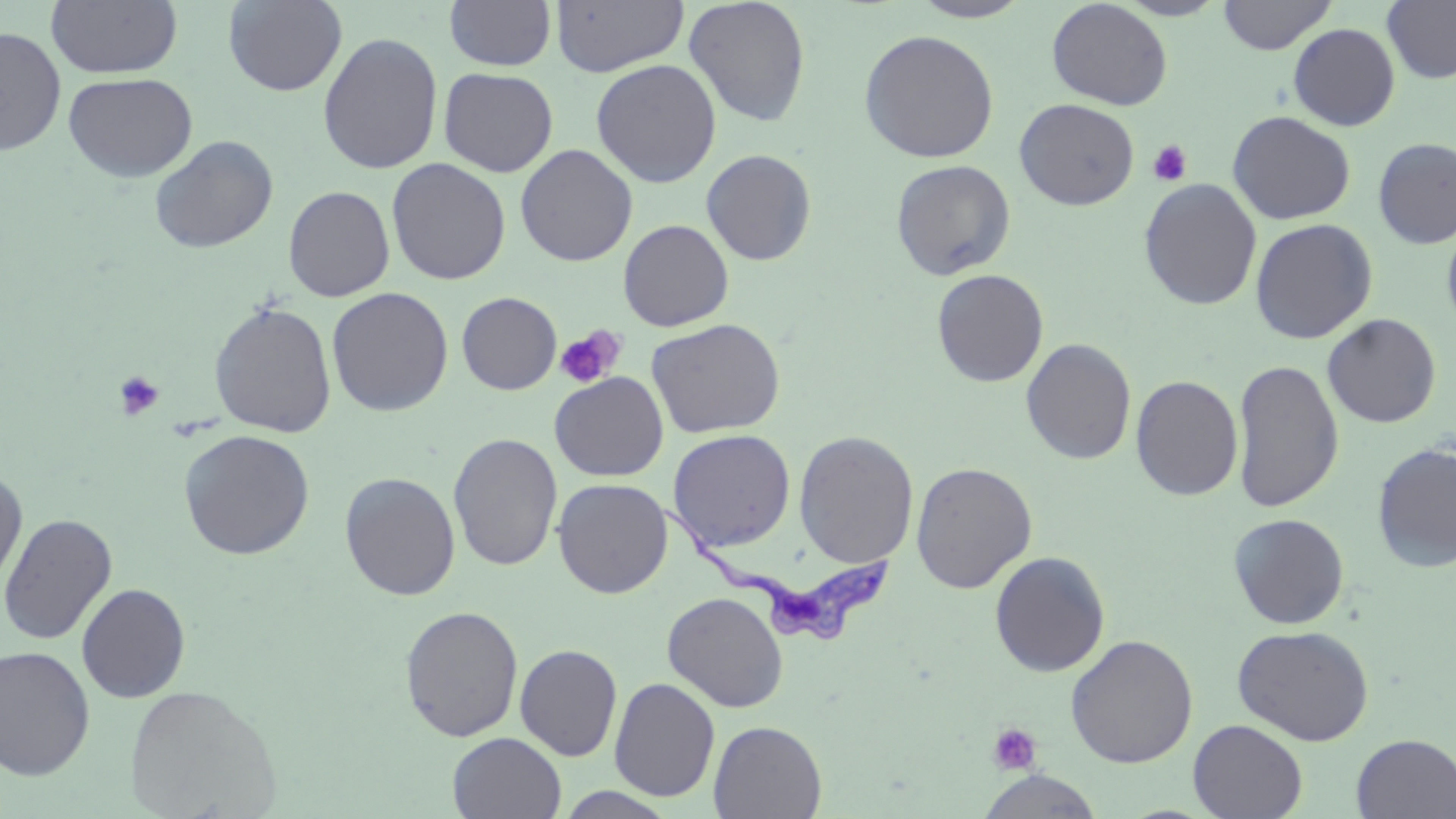

Summary:
  - Coordinate format: approximate bounding boxes as named x1/y1/x2/y2 corners in pixels
  - Trypanosoma brucei locations: (x1=654, y1=497, x2=896, y2=650)
  - Uninfected red blood cell locations: (x1=45, y1=0, x2=183, y2=78), (x1=444, y1=0, x2=557, y2=70), (x1=683, y1=0, x2=811, y2=128), (x1=909, y1=0, x2=1032, y2=22), (x1=1114, y1=0, x2=1230, y2=21), (x1=1218, y1=0, x2=1336, y2=55), (x1=1382, y1=0, x2=1456, y2=85), (x1=223, y1=1, x2=347, y2=96), (x1=550, y1=1, x2=688, y2=76), (x1=1046, y1=1, x2=1173, y2=110), (x1=1287, y1=23, x2=1400, y2=131), (x1=0, y1=25, x2=67, y2=157), (x1=858, y1=29, x2=999, y2=163), (x1=317, y1=32, x2=443, y2=174), (x1=591, y1=58, x2=722, y2=187), (x1=439, y1=67, x2=558, y2=177), (x1=63, y1=71, x2=198, y2=182), (x1=1015, y1=98, x2=1139, y2=210), (x1=1227, y1=110, x2=1355, y2=225), (x1=149, y1=134, x2=279, y2=253), (x1=1373, y1=137, x2=1456, y2=249), (x1=516, y1=143, x2=637, y2=266), (x1=700, y1=149, x2=817, y2=266), (x1=386, y1=158, x2=510, y2=285), (x1=890, y1=159, x2=1016, y2=280), (x1=1139, y1=178, x2=1262, y2=310), (x1=283, y1=185, x2=395, y2=302), (x1=1441, y1=213, x2=1456, y2=338), (x1=1250, y1=218, x2=1377, y2=344), (x1=618, y1=219, x2=734, y2=332), (x1=931, y1=269, x2=1049, y2=388), (x1=326, y1=287, x2=453, y2=416), (x1=456, y1=291, x2=561, y2=395), (x1=208, y1=301, x2=337, y2=438), (x1=1322, y1=313, x2=1441, y2=428), (x1=646, y1=317, x2=786, y2=439), (x1=1021, y1=338, x2=1137, y2=465), (x1=1231, y1=358, x2=1344, y2=513), (x1=550, y1=372, x2=668, y2=481), (x1=1131, y1=375, x2=1244, y2=501), (x1=178, y1=429, x2=315, y2=559), (x1=667, y1=429, x2=796, y2=552), (x1=793, y1=430, x2=919, y2=568), (x1=447, y1=433, x2=563, y2=572), (x1=1372, y1=441, x2=1456, y2=574), (x1=911, y1=461, x2=1037, y2=594), (x1=0, y1=469, x2=28, y2=593), (x1=339, y1=471, x2=460, y2=601), (x1=552, y1=478, x2=673, y2=598), (x1=0, y1=512, x2=117, y2=646), (x1=1228, y1=513, x2=1350, y2=629), (x1=989, y1=551, x2=1110, y2=677), (x1=76, y1=582, x2=191, y2=703), (x1=662, y1=591, x2=788, y2=712), (x1=399, y1=605, x2=524, y2=742), (x1=1232, y1=624, x2=1375, y2=745), (x1=1065, y1=633, x2=1198, y2=768), (x1=514, y1=643, x2=622, y2=761), (x1=0, y1=645, x2=95, y2=779), (x1=609, y1=677, x2=720, y2=802), (x1=124, y1=684, x2=281, y2=818), (x1=1188, y1=719, x2=1307, y2=819), (x1=708, y1=720, x2=827, y2=818), (x1=447, y1=732, x2=567, y2=818), (x1=1351, y1=733, x2=1456, y2=818), (x1=977, y1=770, x2=1104, y2=818), (x1=554, y1=787, x2=679, y2=818)
  - Platelet locations: (x1=1146, y1=139, x2=1193, y2=187), (x1=554, y1=326, x2=626, y2=389), (x1=113, y1=370, x2=164, y2=421), (x1=987, y1=722, x2=1042, y2=776)
  - Slide-level diagnosis: Trypanosoma brucei
  - Field of view: one of a larger specimen
  - Modality: light microscopy
  - Preparation: thin blood film
  - Magnification: 1000x
  - Stain: May-Grünwald-Giemsa
  - Image size: 1456×819 pixels